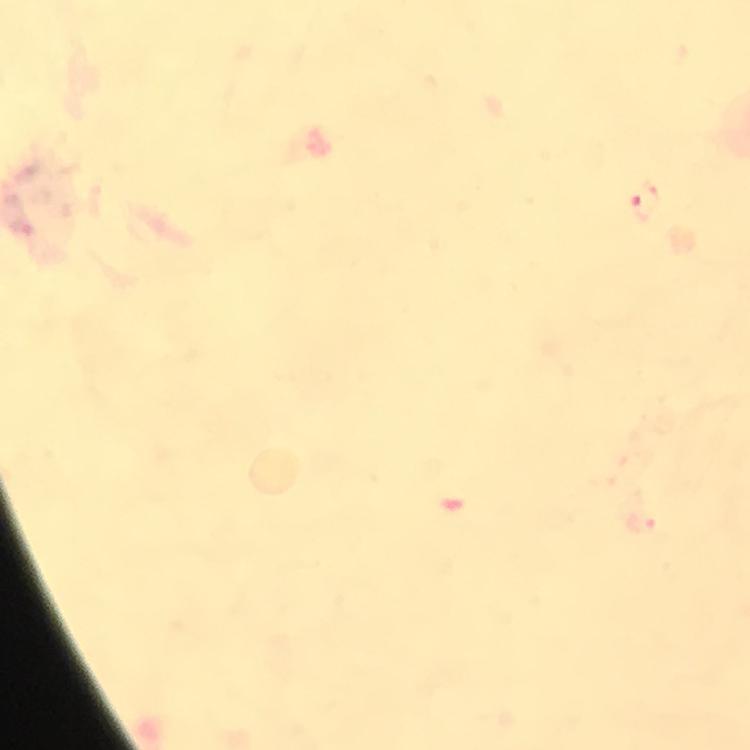

Approximate centers as (x, y) in pixels.
Summary:
  - Malaria parasite locations: (646, 203), (642, 524)
  - Preparation: thick smear
  - Cropped from: one field of view
  - Context: from a diagnostic examination for malaria
  - Immersion oil: used
  - Stain: Giemsa
  - Image size: 750×750 pixels
  - Magnification: 100x
  - Capture: smartphone mounted on the microscope